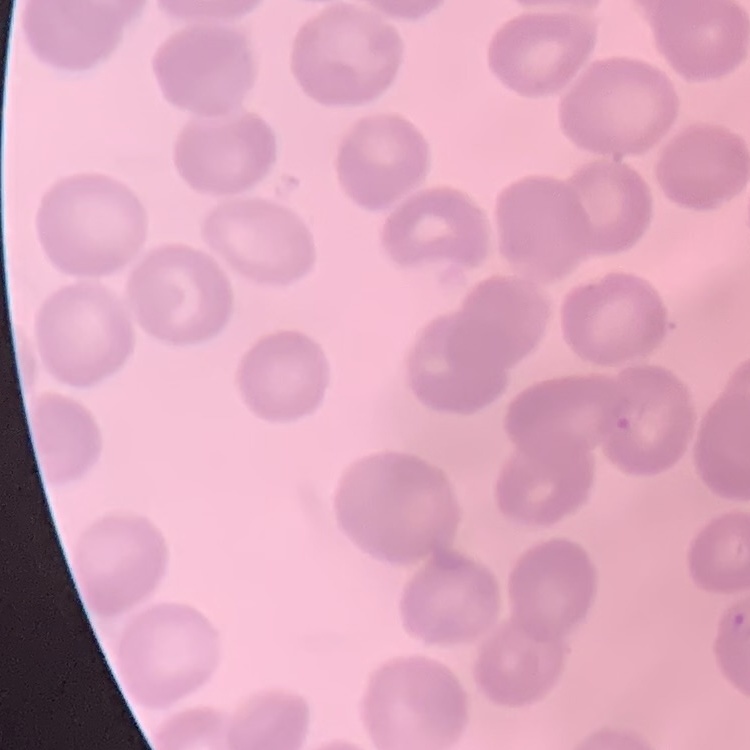

Summary:
  - Red blood cell morphology: no rouleaux formation
  - Image type: square crop of a larger photomicrograph
  - Stain: Field's or Giemsa
  - Preparation: thin blood film